Report the malaria status of this cell.
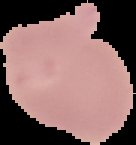

It is uninfected.

Image is 136×145 pixels. From a thin blood film. Segmented cell region on a black background.